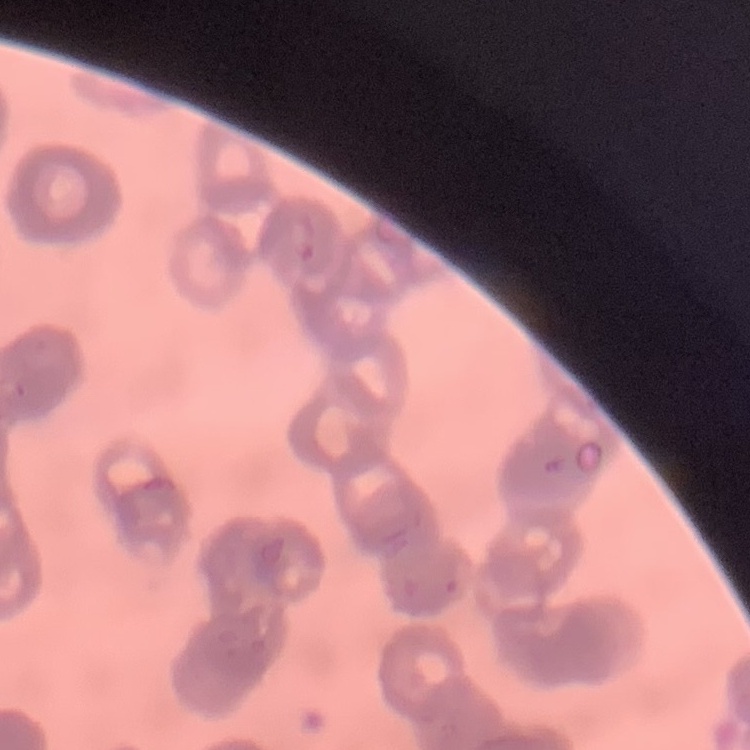

{
  "red_blood_cell_morphology": "rouleaux formation",
  "image_type": "one tile cut from a larger photomicrograph",
  "stain": "Field's or Giemsa",
  "preparation": "thin blood film"
}